Assess this cell for malaria.
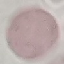
Uninfected.

Summary:
  - Image type: automatically extracted cell patch, resized to 64 × 64 pixels
  - Stain: Giemsa
  - Capture: smartphone through the microscope eyepiece
  - Preparation: thin blood smear